Classify this cell by malaria status.
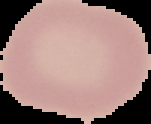

Uninfected.

From a thin blood smear. Image is 151×124 pixels. Cell region segmented out of the field of view; the surrounding area is masked to black.